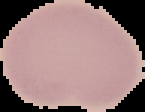
Summary:
  - Preparation: thin blood film
  - Image type: segmented cell region with the area outside set to black
  - Image size: 145×112 pixels
  - Result: no malaria parasites seen